Report the malaria status of this cell.
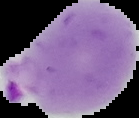
Parasitized.

Summary:
  - Image size: 139×118 pixels
  - Image type: cell region segmented out of the field of view; surrounding area masked to black
  - Preparation: thin blood film